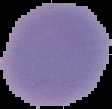

The area outside the segmented cell region is set to black. Malaria status: uninfected. From a thin blood smear. Image is 112×109 pixels.